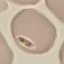
Summary:
  - Result: no malaria parasites seen
  - Capture: smartphone camera at the microscope eyepiece
  - Image type: automatically extracted cell patch, resized to 64 × 64 pixels
  - Stain: Giemsa
  - Preparation: thin smear